Assess this cell for malaria.
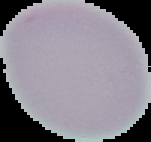

It is uninfected.

image size = 151×142 pixels
image type = cell region segmented out of the field of view; surrounding area masked to black
preparation = thin blood film